Describe the morphology of the red blood cells.
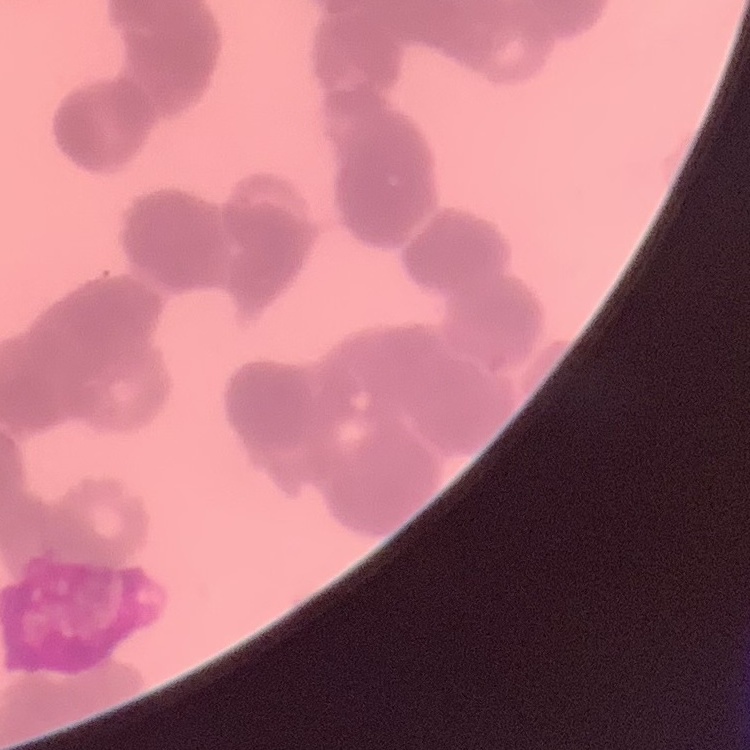
Rouleaux formation.

Summary:
  - Stain: Field's or Giemsa
  - Image type: square crop of a larger photomicrograph
  - Preparation: thin blood film